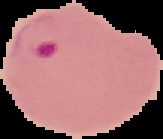 Malaria status: parasitized. The area outside the segmented cell region is set to black. From a thin blood film. Image is 163×139 pixels.